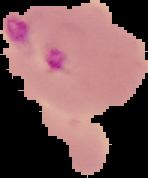 The area outside the segmented cell region is set to black. From a thin blood film. Malaria status: parasitized. Image is 148×178 pixels.